Classify this cell by malaria status.
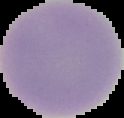

It is uninfected.

The area outside the segmented cell region is set to black. Image is 124×118 pixels. From a thin blood smear.